Outline each Plasmodium falciparum parasite and classify it by life-cycle stage.
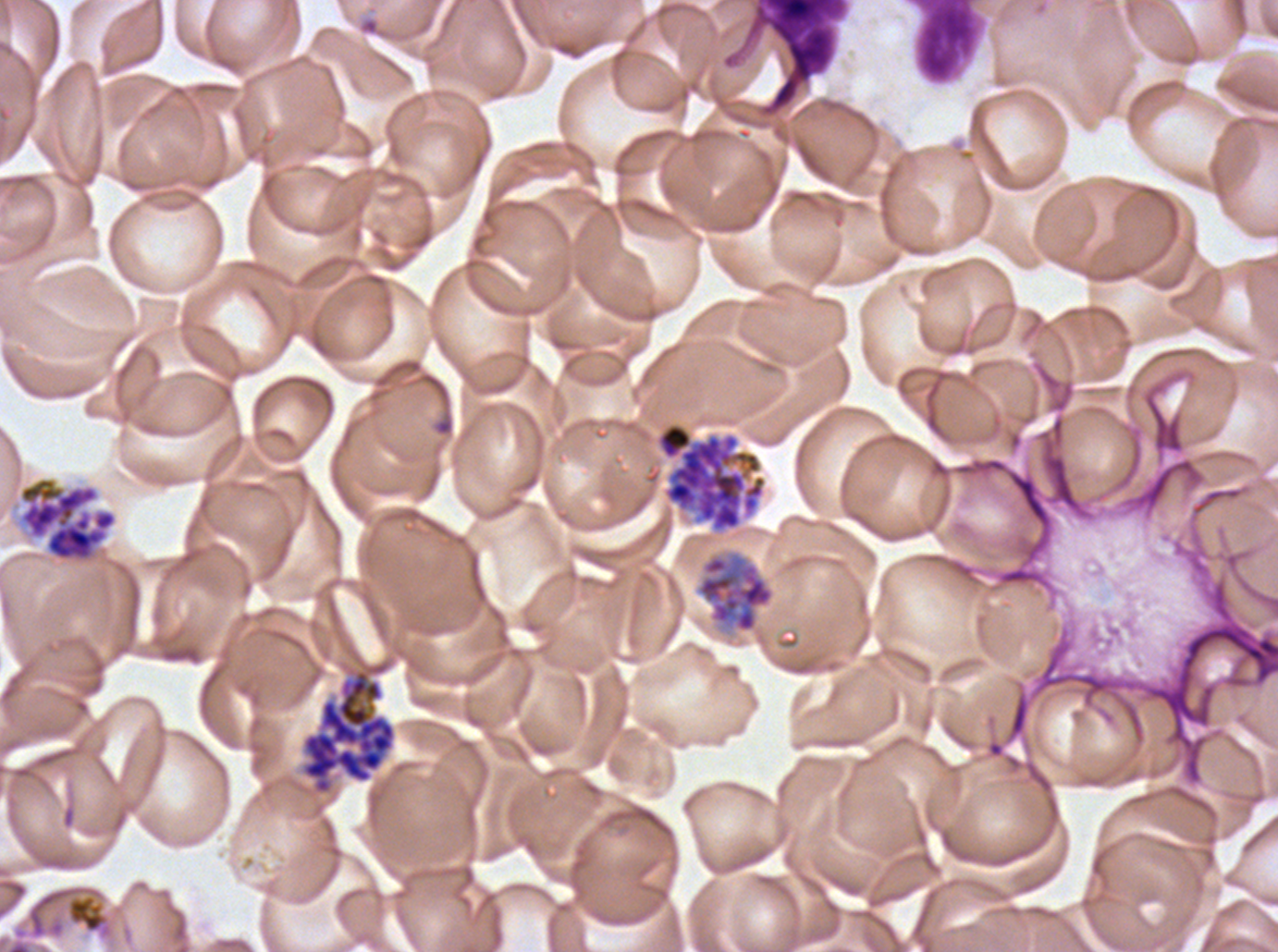

Approximate bounding boxes as {x1, y1, x2, y2} in pixels.
Early schizonts: {696, 554, 774, 633}.
Segmenters: {655, 421, 768, 533}, {18, 477, 117, 562}, {301, 668, 397, 795}.
No rings, late-ring/early-trophozoite forms, mid trophozoites, late trophozoites, late schizonts, or gametocytes observed.

specimen: Plasmodium falciparum cultured ex vivo for 24 to 48 hours, from a patient in The Gambia
image_size: 1278×952 pixels
field_of_view: sub-image separated from a larger composite
life_cycle_stages_observed: early schizont, segmenter
preparation: thin blood film
stain: Giemsa
debris_locations: 'approximate bounding boxes as {x1, y1, x2, y2} in pixels: {0, 883, 126, 951}'
leukocyte_locations: 'approximate bounding boxes as {x1, y1, x2, y2} in pixels: {754, 0, 847, 112}, {910, 0, 981, 84}'